State the blood parasite species.
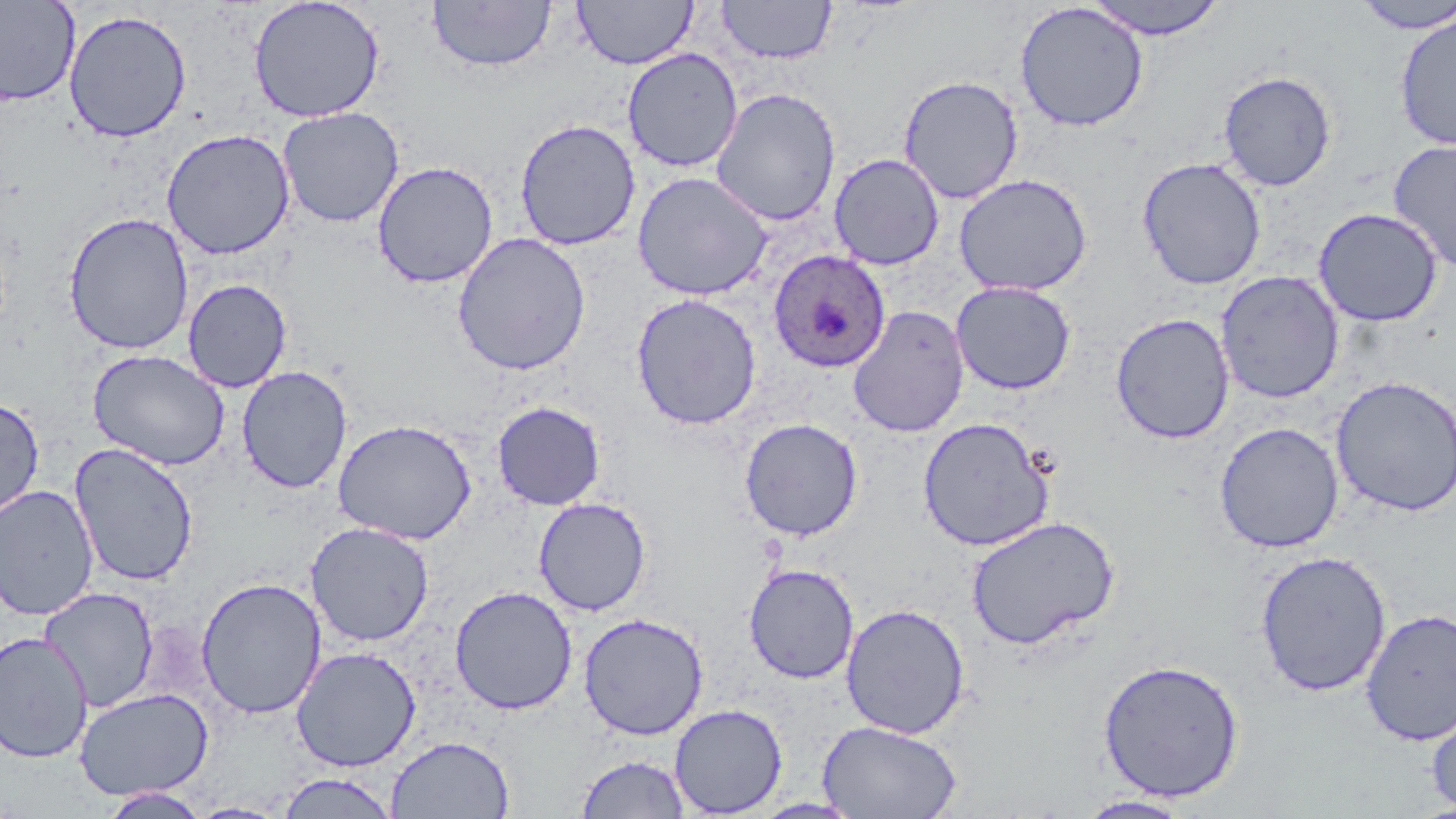
Plasmodium ovale.

Approximate bounding boxes as [x1, y1, x2, y2] in pixels. Uninfected red blood cell locations: [0, 0, 80, 107], [248, 0, 386, 123], [572, 0, 698, 69], [716, 0, 837, 64], [1083, 0, 1231, 40], [427, 1, 557, 73], [1350, 1, 1456, 34], [1014, 2, 1149, 132], [63, 9, 192, 143], [1393, 13, 1456, 151], [622, 48, 743, 173], [1217, 70, 1338, 192], [898, 75, 1023, 204], [710, 87, 842, 227], [277, 107, 404, 228], [514, 118, 641, 251], [161, 128, 296, 260], [1387, 139, 1456, 272], [829, 153, 945, 270], [1136, 157, 1267, 290], [372, 160, 499, 288], [632, 171, 773, 301], [954, 173, 1093, 296], [1313, 207, 1443, 326], [63, 212, 195, 355], [452, 232, 591, 376], [1215, 270, 1345, 404], [182, 278, 292, 392], [951, 280, 1076, 395], [630, 293, 762, 430], [848, 304, 969, 438], [1110, 312, 1235, 444], [88, 349, 230, 470], [236, 365, 353, 494], [1331, 375, 1456, 517], [0, 396, 44, 523], [492, 400, 606, 511], [917, 417, 1056, 551], [332, 418, 477, 545], [739, 418, 864, 541], [1214, 422, 1344, 553], [68, 442, 200, 586], [0, 484, 99, 620], [533, 497, 652, 616], [965, 515, 1121, 651], [306, 522, 434, 646], [1254, 550, 1392, 697], [743, 563, 860, 684], [195, 576, 326, 720], [449, 585, 578, 715], [38, 587, 159, 712], [840, 603, 971, 738], [1360, 608, 1456, 746], [578, 612, 708, 740], [0, 632, 94, 763], [291, 646, 421, 772], [1097, 659, 1245, 802], [74, 688, 213, 800], [1426, 702, 1456, 814], [669, 703, 788, 817], [817, 719, 963, 819], [386, 735, 515, 819], [575, 754, 691, 818], [275, 772, 399, 818], [98, 787, 212, 818], [1074, 795, 1195, 818], [188, 802, 290, 819]. Plasmodium ovale-infected red blood cell locations: [767, 248, 890, 372]. Captured at 1000x magnification. Image is 1456×819 pixels. One field of a larger specimen. May-Grünwald-Giemsa stain. Optical microscopy. Thin blood smear.